Name the parasite shown.
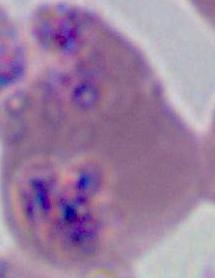

This is Plasmodium.

Photomicrograph. 400x or 1000x magnification.